Report the malaria status of this cell.
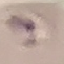
It is uninfected.

Summary:
  - Capture: smartphone through the microscope eyepiece
  - Stain: Giemsa
  - Image type: automatically extracted cell patch, resized to 64 × 64 pixels
  - Preparation: thin blood smear